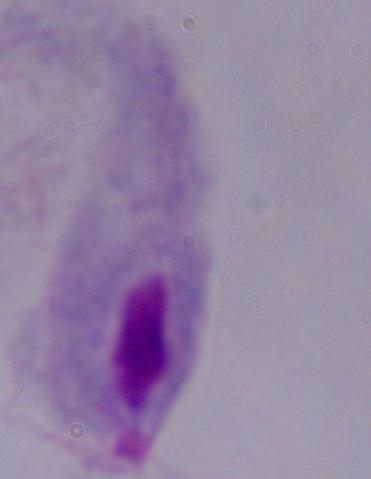
Summary:
  - Modality: photomicrograph
  - Identification: trichomonad
  - Magnification: 1000x